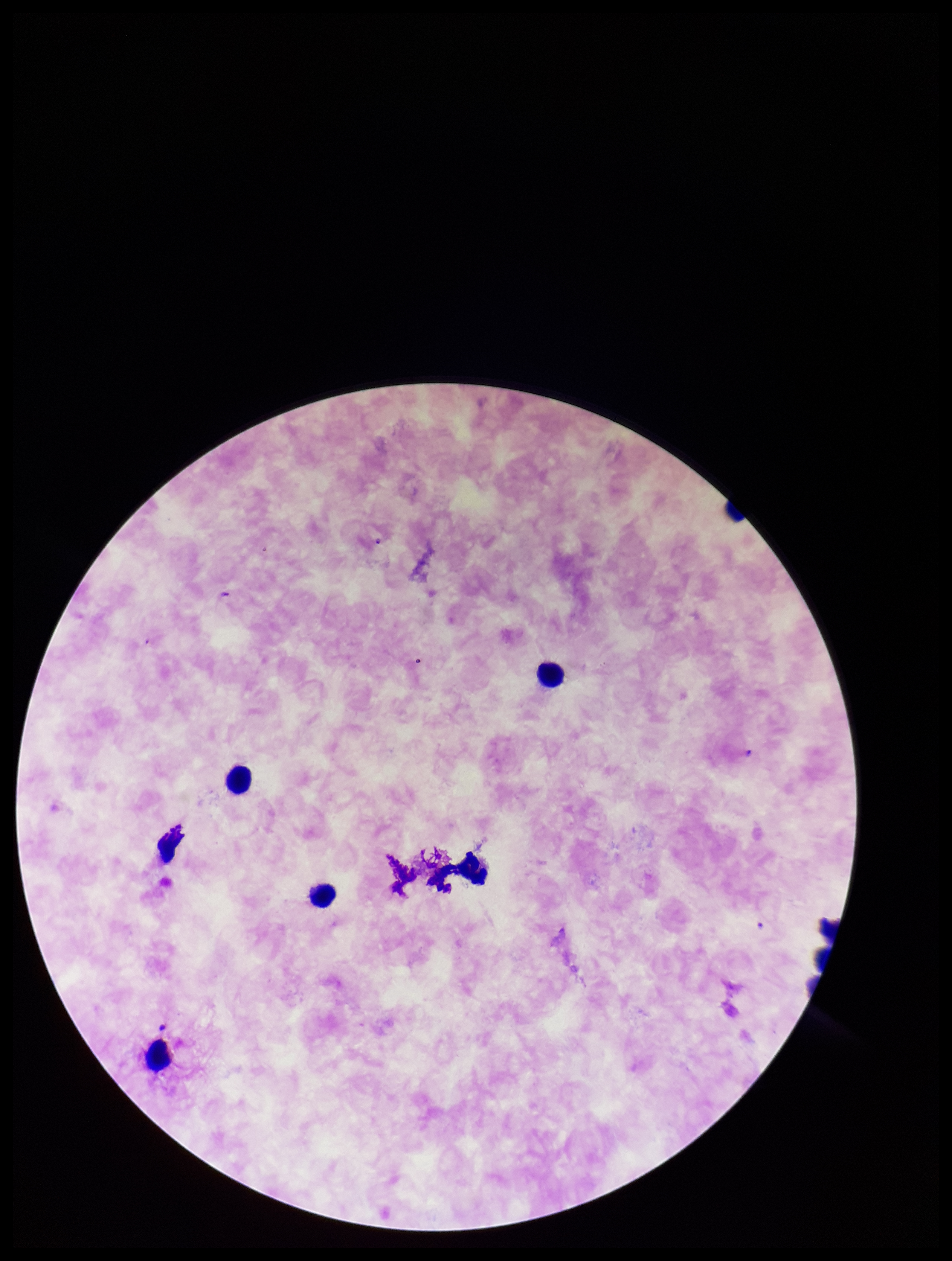 Leukocyte count: 6. Patient malaria status: infected. Stained with Giemsa. Plasmodium parasites: none detected. Image is 952×1261 pixels. One field from this slide. Preparation: thick smear. Parasite count: 0. Smartphone photograph taken through the eyepiece of a microscope. Species reported for this patient: Plasmodium falciparum.